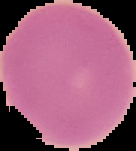

{
  "preparation": "thin blood film",
  "malaria_status": "uninfected",
  "image_type": "segmented cell region with the area outside set to black",
  "image_size": "136×151 pixels"
}